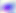
Photomicrograph. Toxoplasma gondii is seen. Captured at 400x magnification.